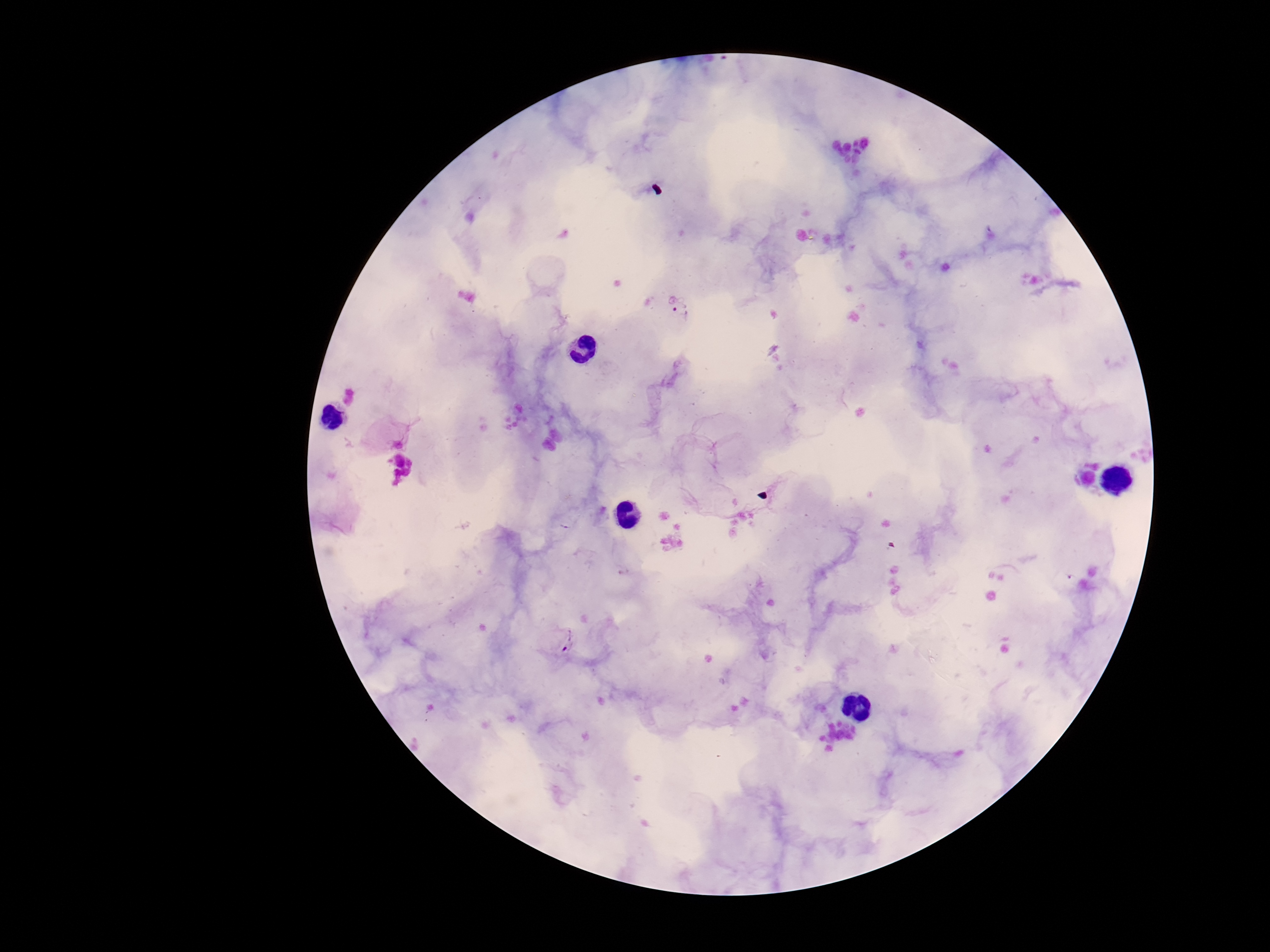

{
  "magnification": "100x",
  "capture": "smartphone camera through the microscope eyepiece",
  "image_size": "1270×952 pixels",
  "patient_malaria_status": "positive",
  "preparation": "thick blood smear",
  "field_of_view": "single",
  "plasmodium_parasite_locations": "approximate centers as [x, y] in pixels: [680, 310], [560, 639]",
  "stain": "Giemsa"
}